Locate every blood parasite and identify its species.
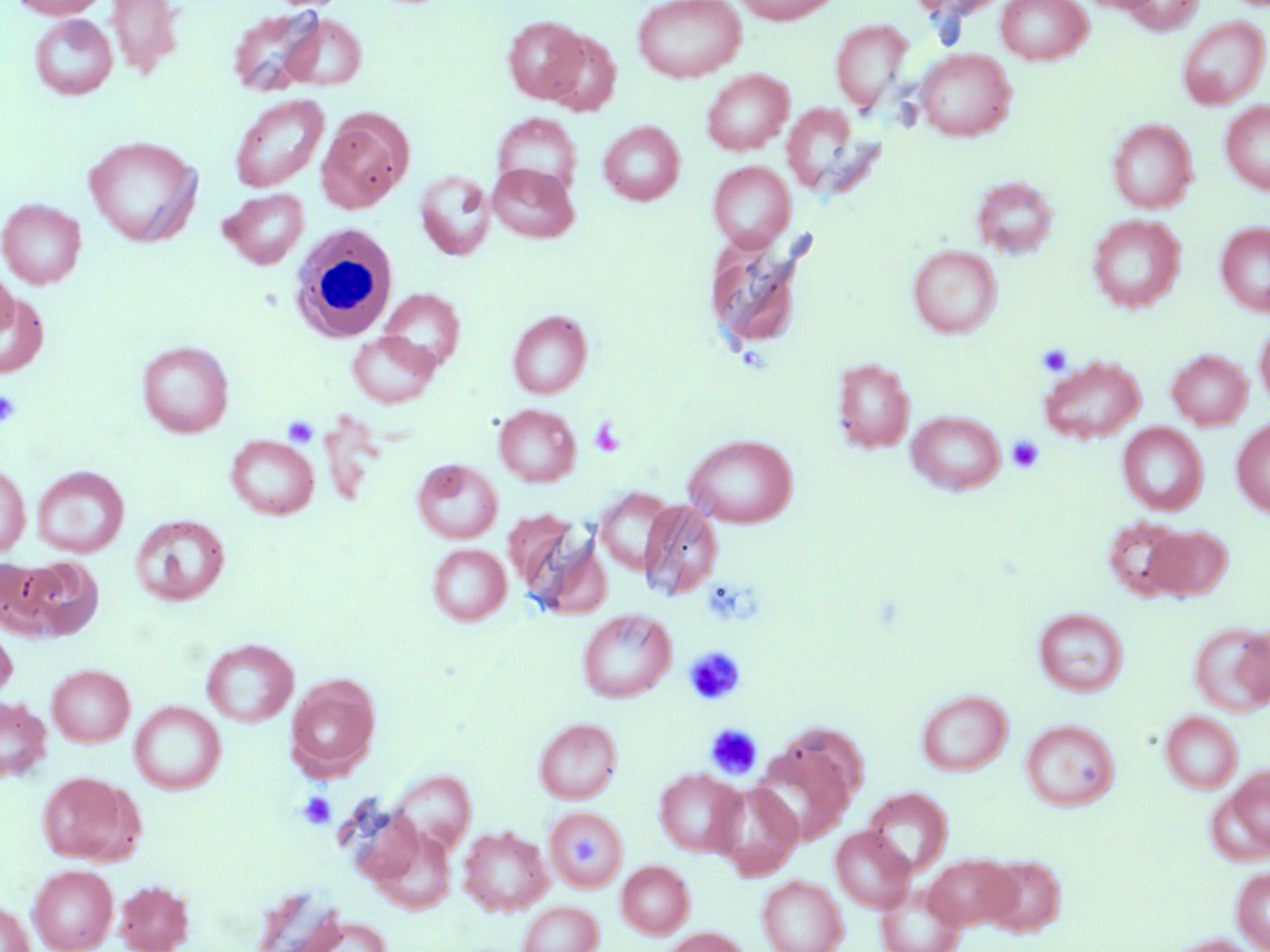

No blood parasites seen.

{
  "slide_level_diagnosis": "no evidence of blood parasites",
  "image_size": "1270×952 pixels",
  "stain": "May-Grünwald-Giemsa",
  "uninfected_red_blood_cell_locations": "approximate bounding boxes as (x1,y1)-(x2,y2) corner pairs in pixels: (10,0)-(110,19), (105,0)-(185,79), (632,0)-(746,83), (732,0)-(840,24), (909,0)-(1012,20), (996,0)-(1092,65), (1121,0)-(1204,34), (228,5)-(326,97), (30,14)-(117,100), (281,15)-(367,90), (503,16)-(589,103), (1177,17)-(1269,109), (830,20)-(912,109), (540,29)-(621,116), (916,49)-(1016,141), (701,69)-(793,155), (229,93)-(329,193), (1220,101)-(1270,195), (781,103)-(873,197), (317,112)-(411,212), (492,113)-(581,196), (1107,118)-(1197,213), (598,121)-(685,206), (83,136)-(202,246), (707,161)-(796,250), (487,163)-(580,243), (414,170)-(495,260), (972,176)-(1059,259), (219,188)-(309,269), (0,198)-(86,289), (1087,214)-(1185,312), (1216,222)-(1270,316), (704,234)-(807,351), (908,245)-(1002,338), (0,267)-(18,339), (378,288)-(465,372), (0,290)-(50,377), (507,310)-(592,398), (1255,320)-(1270,411), (347,331)-(439,408), (136,341)-(234,437), (1167,349)-(1252,430), (1040,355)-(1145,444), (832,358)-(915,453), (493,404)-(581,486), (906,410)-(1006,495), (1231,417)-(1270,516), (1118,422)-(1208,514), (683,433)-(799,528), (226,435)-(319,520), (412,458)-(503,543), (0,461)-(31,557), (31,466)-(129,557), (594,487)-(675,575), (639,499)-(722,601), (131,514)-(230,605), (1103,516)-(1194,600), (515,522)-(610,619), (1144,526)-(1232,601), (427,543)-(511,626), (18,556)-(104,640), (577,608)-(675,703), (1034,608)-(1129,696), (0,620)-(17,701), (1189,622)-(1270,715), (202,638)-(298,727), (47,664)-(134,746), (286,674)-(381,778), (917,689)-(1012,776), (0,696)-(52,782), (129,701)-(226,794), (1160,711)-(1242,793), (533,717)-(623,804), (1020,719)-(1119,811), (750,744)-(854,847), (1219,766)-(1270,857), (654,768)-(744,857), (389,769)-(476,853), (36,771)-(139,864), (710,781)-(802,879), (863,787)-(953,877), (544,806)-(628,892), (368,825)-(457,916), (459,826)-(552,916), (830,826)-(915,912), (924,854)-(1018,930), (982,855)-(1066,936), (617,860)-(694,938), (28,864)-(118,952), (1232,867)-(1270,951), (757,876)-(848,952), (114,879)-(195,952), (876,883)-(966,952), (517,901)-(603,952), (0,902)-(34,952), (289,914)-(394,952), (661,927)-(750,952), (1165,934)-(1260,952)",
  "magnification": "1000x",
  "field_of_view": "single",
  "platelet_locations": "approximate bounding boxes as (x1,y1)-(x2,y2) corner pairs in pixels: (1037,343)-(1073,376), (0,390)-(21,428), (283,415)-(319,448), (588,417)-(626,457), (1007,436)-(1044,473), (684,646)-(746,705), (706,723)-(763,779), (298,791)-(336,829), (566,835)-(604,868)",
  "white_blood_cell_locations": "approximate bounding boxes as (x1,y1)-(x2,y2) corner pairs in pixels: (287,223)-(398,343)",
  "modality": "light microscopy",
  "preparation": "thin blood smear"
}